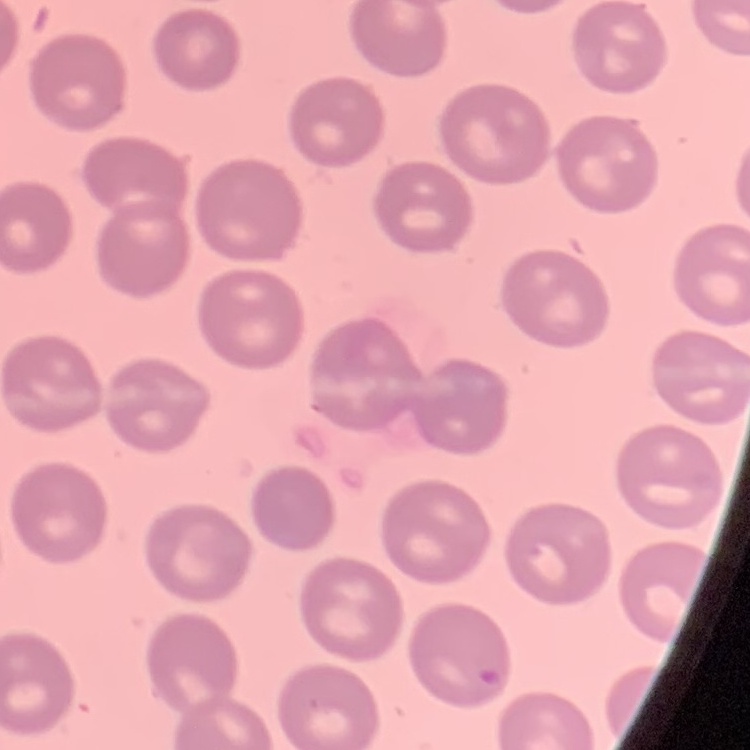 The red blood cells show no rouleaux formation. One tile cut from a larger photomicrograph. Stained with either Field's or Giemsa. Thin blood smear.